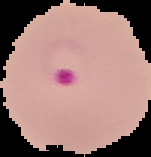
Summary:
  - Image size: 151×157 pixels
  - Preparation: thin blood smear
  - Image type: segmented cell region with the area outside set to black
  - Malaria status: parasitized